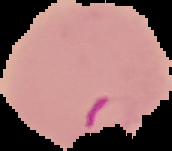
Malaria status: parasitized. Image is 172×151 pixels. Segmented cell region on a black background. From a thin blood smear.